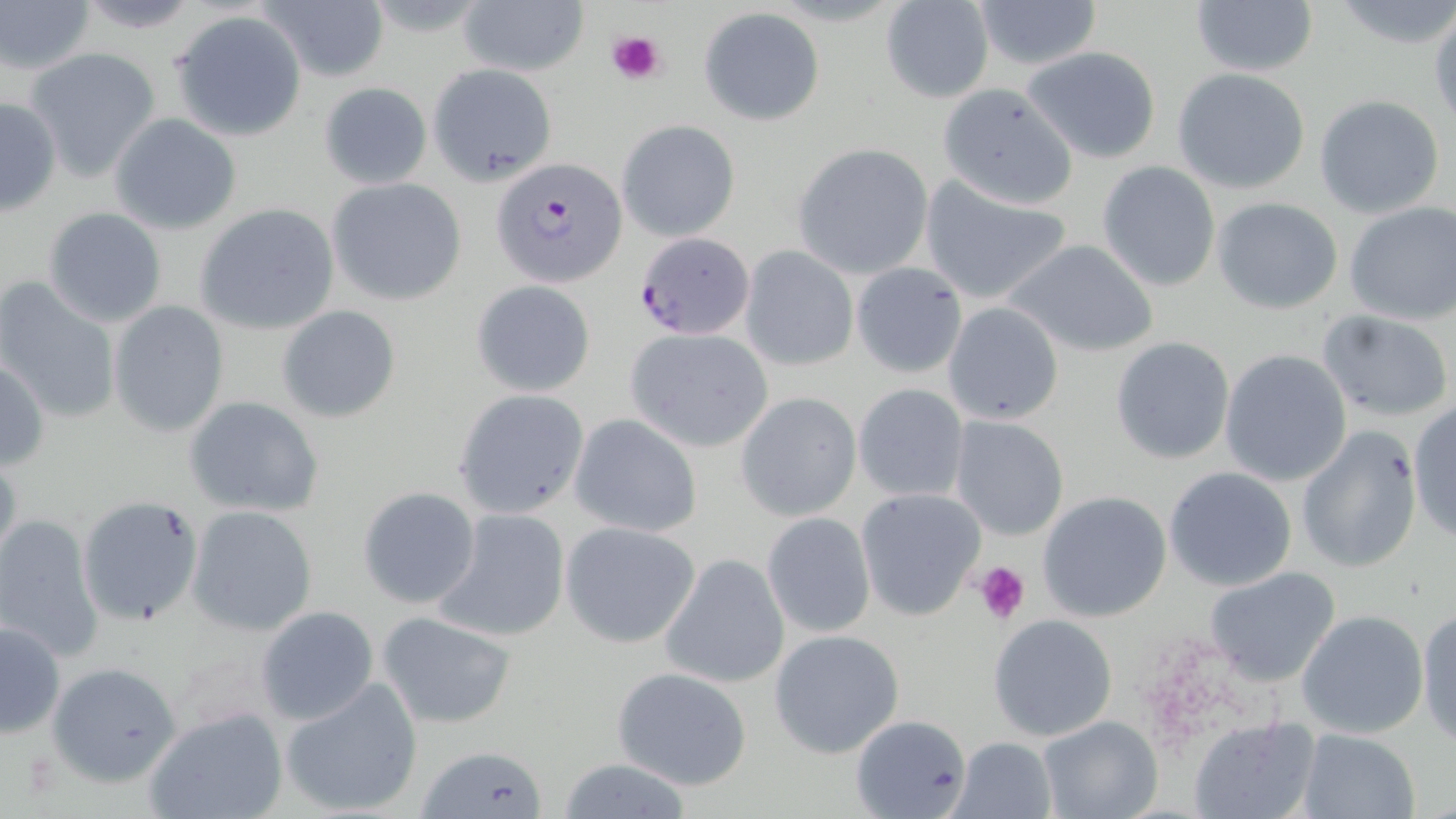

{
  "slide_level_diagnosis": "Plasmodium falciparum",
  "modality": "light microscopy",
  "platelet_locations": "approximate bounding boxes as (x1, y1, x2, y2) in pixels: (603, 28, 668, 86), (974, 561, 1032, 624)",
  "magnification": "1000x",
  "preparation": "thin blood smear",
  "image_size": "1456×819 pixels",
  "plasmodium_falciparum_infected_red_blood_cell_locations": "approximate bounding boxes as (x1, y1, x2, y2) in pixels: (493, 158, 627, 285), (633, 233, 756, 342)",
  "stain": "May-Grünwald-Giemsa",
  "uninfected_red_blood_cell_locations": "approximate bounding boxes as (x1, y1, x2, y2) in pixels: (72, 0, 203, 32), (256, 0, 390, 82), (457, 0, 589, 80), (969, 0, 1106, 70), (1187, 0, 1318, 79), (1, 1, 97, 78), (1330, 1, 1456, 50), (879, 2, 995, 103), (698, 6, 825, 125), (1429, 11, 1456, 129), (171, 14, 306, 138), (1021, 45, 1162, 163), (25, 48, 163, 181), (429, 63, 559, 186), (1172, 68, 1312, 195), (318, 82, 433, 189), (937, 82, 1079, 209), (1313, 94, 1446, 219), (0, 96, 61, 217), (109, 113, 241, 235), (616, 119, 740, 242), (791, 143, 933, 280), (1096, 161, 1221, 291), (326, 178, 468, 306), (919, 179, 1073, 307), (1211, 198, 1346, 315), (1342, 201, 1456, 324), (195, 202, 340, 336), (42, 208, 168, 328), (1002, 238, 1162, 358), (740, 247, 858, 371), (850, 262, 969, 378), (0, 280, 122, 425), (470, 280, 596, 397), (942, 301, 1064, 426), (109, 302, 229, 437), (278, 306, 401, 423), (1318, 309, 1454, 421), (626, 328, 773, 452), (1110, 337, 1235, 464), (1219, 347, 1352, 487), (0, 356, 48, 473), (851, 381, 971, 503), (453, 389, 589, 520), (736, 393, 861, 522), (183, 396, 324, 519), (1408, 400, 1456, 543), (568, 413, 704, 538), (948, 417, 1070, 541), (1296, 425, 1422, 576), (0, 450, 23, 570), (1163, 467, 1297, 591), (357, 486, 482, 610), (855, 488, 985, 620), (1035, 491, 1173, 624), (76, 494, 204, 626), (186, 506, 317, 636), (431, 508, 571, 644), (0, 513, 103, 663), (760, 513, 877, 639), (558, 520, 702, 649), (659, 552, 790, 689), (1202, 564, 1341, 688), (254, 605, 379, 726), (1415, 605, 1456, 746), (1296, 608, 1429, 740), (376, 611, 519, 729), (987, 614, 1118, 742), (1, 619, 66, 740), (769, 630, 907, 760), (46, 661, 183, 788), (611, 667, 752, 790), (279, 676, 426, 816), (142, 706, 287, 819), (849, 714, 972, 819), (1037, 714, 1162, 819), (1189, 717, 1318, 819), (1295, 729, 1421, 819), (950, 736, 1057, 819), (422, 743, 548, 819), (553, 758, 697, 817)",
  "field_of_view": "single"
}